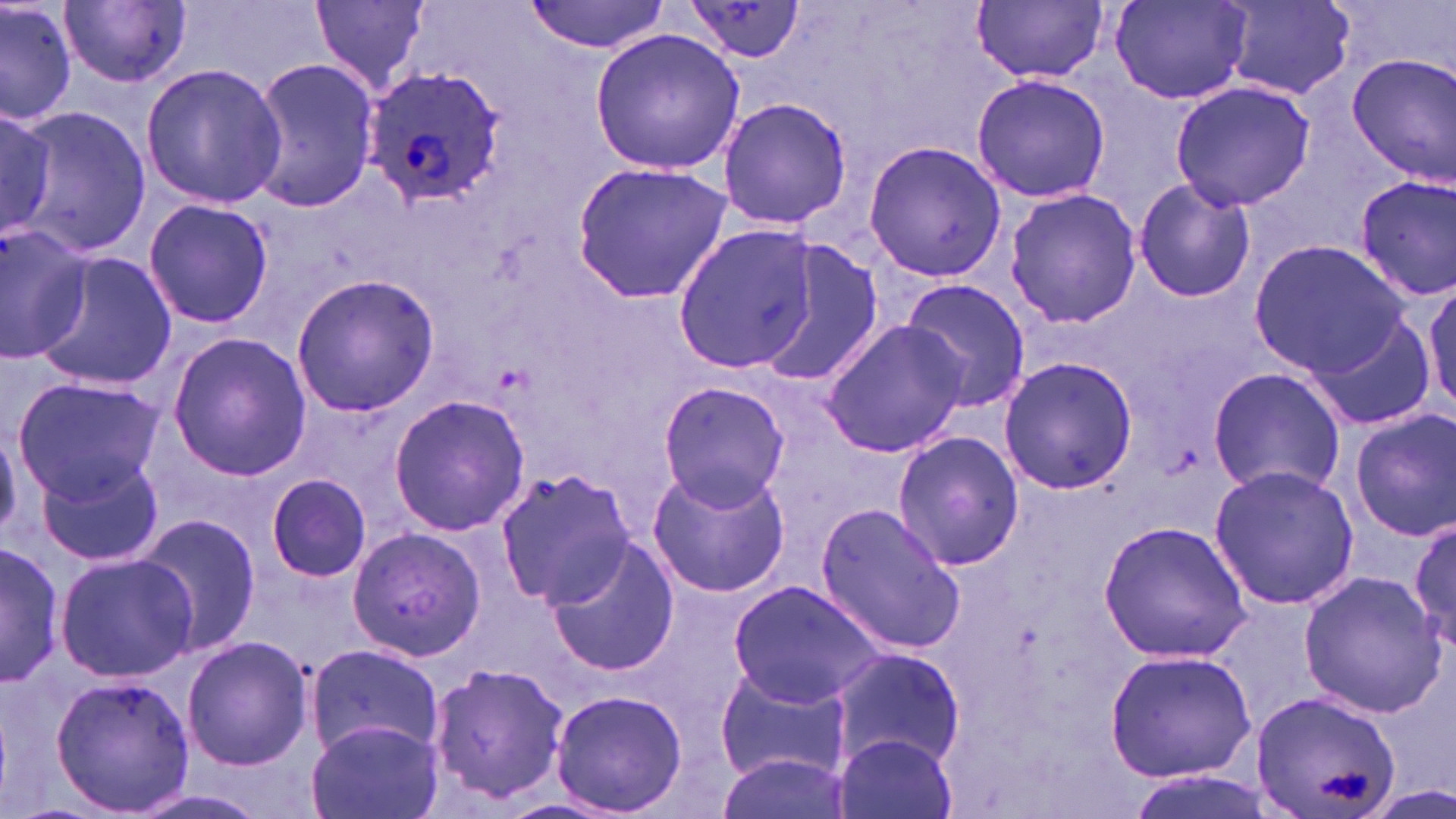

slide_level_diagnosis: Plasmodium ovale
magnification: 1000x
stain: May-Grünwald-Giemsa
platelet_locations: 'approximate bounding boxes as (x1, y1, x2, y2) in pixels: (1318, 770, 1372, 803)'
preparation: thin blood smear
uninfected_red_blood_cell_locations: 'approximate bounding boxes as (x1, y1, x2, y2) in pixels: (0, 0, 76, 128), (309, 0, 431, 94), (1109, 0, 1251, 103), (61, 1, 191, 88), (526, 1, 670, 55), (973, 1, 1108, 84), (1220, 1, 1359, 98), (683, 2, 805, 64), (590, 29, 746, 174), (1347, 53, 1456, 184), (250, 57, 378, 212), (139, 61, 288, 208), (970, 73, 1111, 205), (1167, 80, 1316, 212), (718, 96, 855, 230), (14, 107, 154, 257), (863, 139, 1005, 283), (568, 159, 733, 308), (1352, 173, 1454, 302), (1132, 177, 1255, 304), (1002, 187, 1142, 328), (142, 198, 274, 329), (675, 223, 816, 373), (0, 224, 90, 359), (753, 238, 883, 390), (1249, 240, 1406, 375), (32, 251, 178, 393), (290, 271, 440, 419), (1423, 273, 1455, 420), (898, 279, 1030, 412), (1310, 308, 1436, 431), (820, 317, 969, 458), (165, 332, 313, 480), (996, 354, 1138, 496), (1209, 366, 1346, 498), (11, 373, 162, 502), (654, 380, 791, 511), (388, 393, 529, 537), (1349, 408, 1456, 540), (889, 429, 1025, 574), (35, 453, 166, 567), (647, 463, 791, 598), (1207, 464, 1361, 609), (495, 466, 634, 610), (264, 474, 374, 586), (814, 502, 965, 654), (134, 514, 261, 658), (1411, 516, 1455, 649), (1097, 521, 1251, 661), (346, 528, 486, 661), (544, 537, 678, 676), (1, 541, 63, 688), (54, 551, 198, 683), (1298, 570, 1447, 717), (729, 580, 889, 708), (181, 636, 312, 770), (303, 644, 443, 756), (828, 644, 966, 771), (1103, 647, 1257, 783), (428, 662, 570, 801), (715, 664, 850, 785), (50, 673, 196, 813), (549, 688, 688, 818), (1249, 690, 1402, 815), (306, 720, 442, 819), (835, 730, 958, 819), (716, 748, 845, 819)'
plasmodium_ovale_infected_red_blood_cell_locations: 'approximate bounding boxes as (x1, y1, x2, y2) in pixels: (360, 64, 511, 209)'
image_size: 1456×819 pixels
modality: optical microscopy
field_of_view: one of a larger specimen